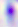
identification = Toxoplasma gondii
modality = micrograph
magnification = 400x